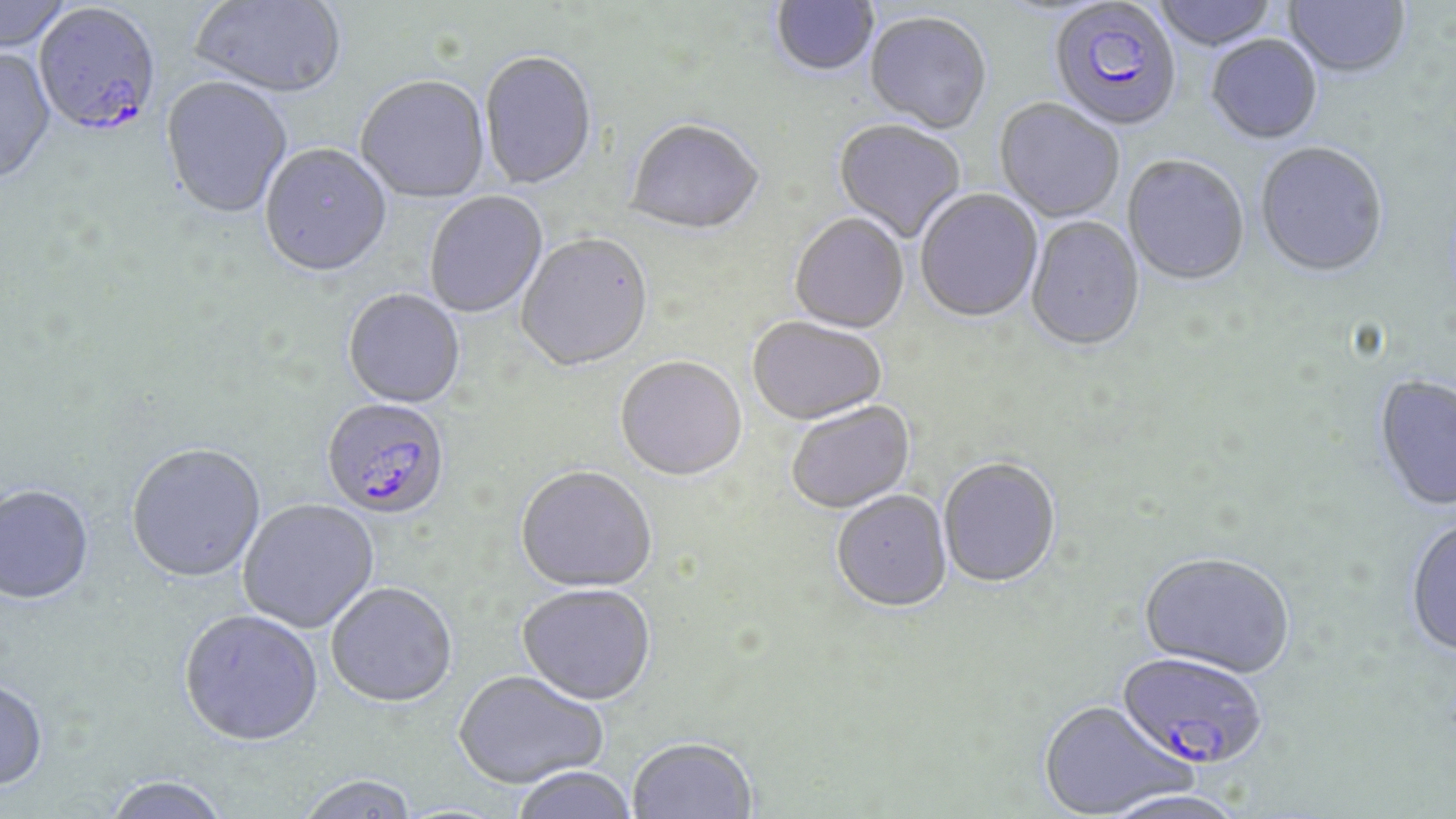

Approximate bounding boxes as (x1, y1, x2, y2) in pixels. Plasmodium falciparum-infected red blood cell locations: (1049, 3, 1182, 134), (33, 5, 163, 142), (322, 399, 451, 521), (1115, 654, 1268, 773). Uninfected red blood cell locations: (1, 0, 75, 55), (189, 0, 348, 101), (771, 0, 879, 79), (1151, 0, 1279, 53), (1283, 0, 1410, 81), (865, 14, 991, 136), (1206, 37, 1322, 146), (0, 49, 57, 188), (479, 53, 597, 192), (356, 78, 490, 205), (159, 79, 293, 222), (995, 100, 1124, 224), (833, 121, 966, 244), (626, 122, 764, 238), (259, 145, 393, 280), (1255, 145, 1389, 281), (1122, 157, 1249, 288), (915, 189, 1043, 325), (425, 191, 548, 319), (789, 215, 909, 336), (1026, 217, 1144, 354), (516, 235, 653, 374), (342, 291, 466, 410), (748, 318, 886, 427), (615, 359, 747, 484), (1374, 376, 1456, 513), (787, 402, 916, 515), (126, 445, 266, 585), (938, 459, 1061, 590), (516, 469, 657, 595), (0, 487, 95, 607), (832, 492, 952, 615), (238, 500, 380, 634), (1405, 519, 1456, 659), (1139, 555, 1295, 681), (326, 584, 457, 710), (517, 586, 656, 708), (179, 611, 324, 750), (453, 672, 608, 791), (0, 681, 49, 794), (1038, 703, 1191, 818), (628, 740, 757, 819), (513, 768, 637, 819), (298, 777, 419, 818), (102, 778, 230, 819), (1101, 791, 1248, 819). Slide-level diagnosis: Plasmodium falciparum. Light microscopy. Thin blood smear. Image is 1456×819 pixels. Single field of view. May-Grünwald-Giemsa-stained preparation. Captured at 1000x magnification.